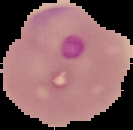
Image is 133×130 pixels. The area outside the segmented cell region is set to black. Malaria status: parasitized. From a thin blood film.